Identify the parasite.
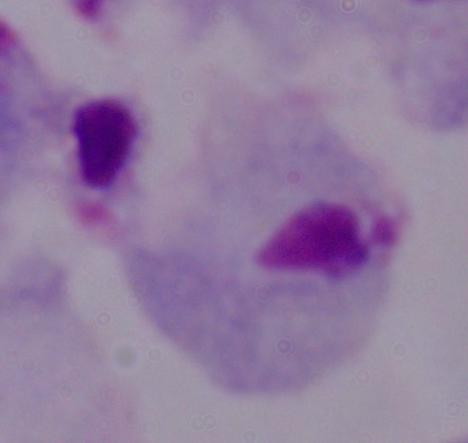
This is a trichomonad.

{
  "magnification": "1000x",
  "modality": "micrograph"
}